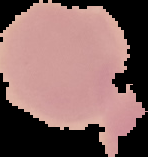

Summary:
  - Result: no Plasmodium parasites seen
  - Image type: segmented cell region on a black background
  - Preparation: thin blood film
  - Image size: 148×157 pixels